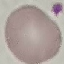

Summary:
  - Result: no malaria parasites seen
  - Preparation: thin blood smear
  - Stain: Giemsa
  - Capture: smartphone camera at the microscope eyepiece
  - Image type: automatically extracted cell patch, resized to 64 × 64 pixels